Identify the blood parasite species.
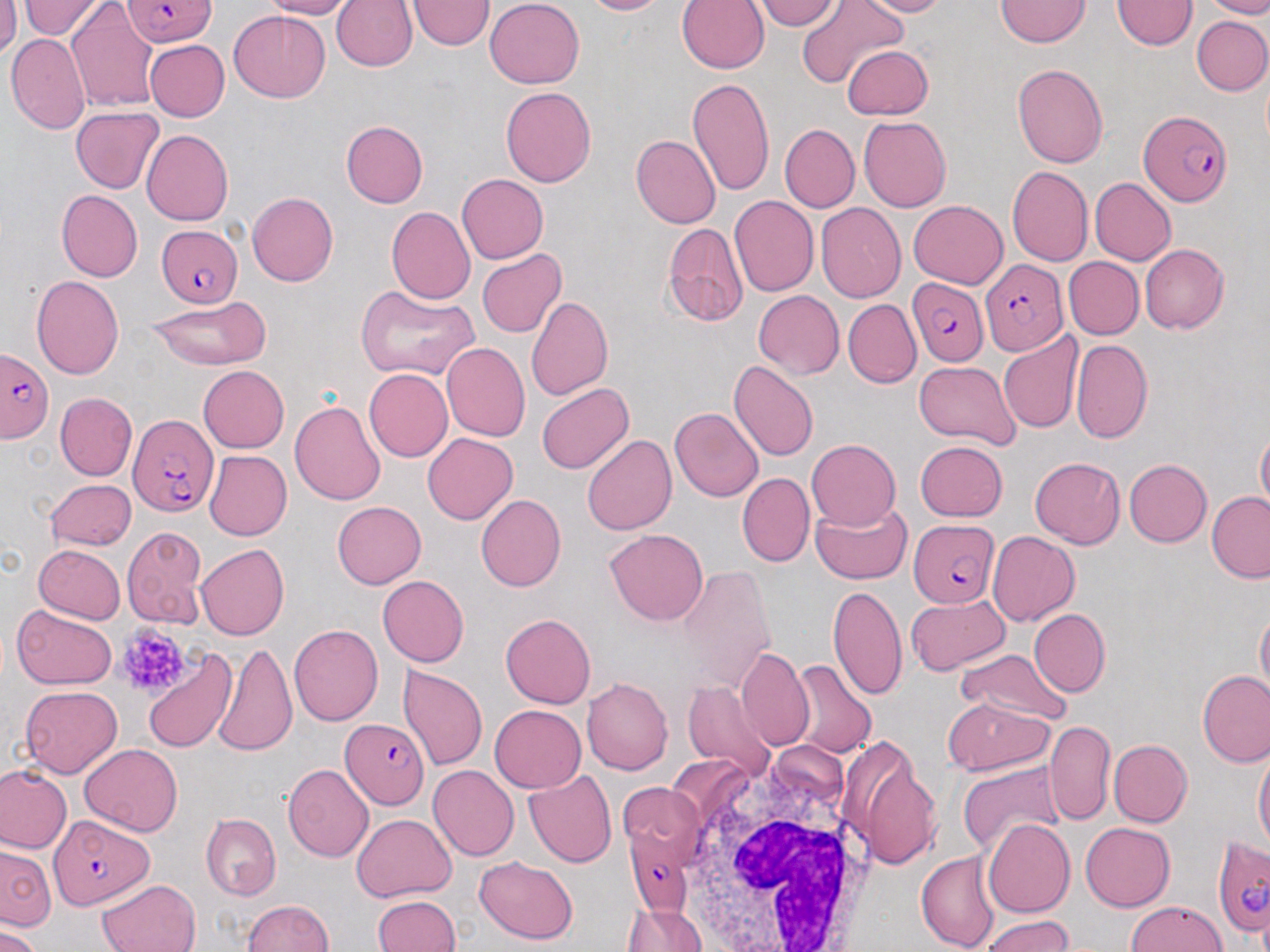
Plasmodium falciparum.

Approximate bounding boxes as (x1, y1, x2, y2) in pixels. Plasmodium falciparum-infected red blood cell locations: (118, 2, 217, 47), (1138, 110, 1234, 207), (154, 223, 243, 308), (981, 259, 1067, 353), (906, 278, 988, 368), (0, 345, 54, 438), (126, 413, 218, 519), (908, 519, 1000, 608), (343, 721, 431, 807), (48, 818, 154, 910), (626, 820, 698, 936), (1213, 837, 1269, 934). Platelet locations: (116, 623, 191, 696). Uninfected red blood cell locations: (17, 0, 106, 42), (261, 0, 355, 18), (330, 0, 417, 73), (410, 0, 490, 50), (581, 0, 673, 18), (676, 0, 769, 74), (754, 0, 844, 30), (858, 0, 956, 16), (996, 0, 1088, 48), (1114, 0, 1195, 52), (1208, 0, 1269, 17), (485, 1, 584, 89), (796, 2, 906, 91), (1, 3, 20, 59), (68, 6, 159, 109), (228, 9, 332, 103), (1191, 15, 1270, 95), (7, 32, 91, 134), (145, 39, 229, 120), (841, 45, 935, 119), (1012, 62, 1107, 168), (687, 78, 774, 196), (500, 85, 596, 189), (73, 106, 164, 192), (860, 114, 953, 213), (342, 122, 428, 207), (778, 123, 860, 215), (141, 130, 234, 224), (630, 136, 719, 229), (1008, 167, 1092, 267), (455, 173, 549, 263), (1089, 178, 1177, 265), (56, 190, 143, 281), (247, 191, 338, 285), (728, 197, 818, 298), (909, 199, 1009, 288), (816, 203, 906, 302), (387, 207, 476, 306), (661, 222, 748, 327), (1140, 244, 1228, 334), (476, 247, 565, 338), (1064, 256, 1144, 337), (31, 272, 125, 380), (354, 284, 481, 384), (753, 291, 845, 379), (146, 296, 273, 368), (525, 298, 616, 401), (842, 299, 921, 390), (998, 331, 1082, 434), (1072, 337, 1153, 443), (441, 342, 530, 442), (914, 360, 1020, 449), (728, 361, 818, 461), (197, 365, 289, 453), (362, 367, 451, 461), (536, 382, 634, 474), (57, 393, 136, 482), (291, 399, 385, 506), (671, 407, 763, 503), (1255, 430, 1269, 514), (423, 433, 517, 524), (581, 433, 677, 537), (806, 438, 900, 531), (915, 440, 1008, 521), (204, 451, 291, 539), (1028, 456, 1125, 549), (1122, 459, 1211, 548), (738, 472, 814, 567), (44, 480, 135, 549), (1207, 491, 1270, 582), (476, 496, 565, 592), (809, 499, 915, 584), (331, 500, 425, 589), (122, 526, 209, 628), (605, 528, 709, 625), (987, 530, 1079, 626), (195, 544, 290, 639), (33, 545, 126, 623), (376, 575, 467, 666), (828, 583, 910, 704), (906, 593, 1013, 675), (11, 606, 119, 688), (1255, 606, 1269, 692), (1029, 609, 1110, 695), (500, 613, 594, 709), (290, 623, 383, 726), (212, 640, 302, 756), (736, 646, 814, 749), (143, 647, 238, 753), (954, 647, 1072, 726), (789, 658, 876, 761), (399, 667, 487, 771), (1198, 672, 1270, 767), (682, 678, 776, 776), (581, 680, 672, 776), (20, 684, 123, 777), (942, 698, 1054, 776), (489, 706, 585, 792), (1045, 719, 1115, 824), (839, 735, 942, 870), (1108, 739, 1192, 828), (80, 744, 181, 836), (1253, 753, 1268, 855), (958, 762, 1068, 857), (0, 763, 69, 854), (283, 764, 373, 863), (427, 765, 518, 859), (526, 771, 619, 867), (617, 783, 705, 856), (199, 813, 281, 900), (351, 813, 457, 902), (981, 817, 1075, 920), (1078, 822, 1174, 912), (1, 845, 56, 934), (916, 850, 1000, 952), (475, 856, 576, 943), (96, 878, 199, 952), (372, 895, 463, 952), (241, 898, 338, 952), (1123, 898, 1229, 952), (626, 902, 708, 952), (978, 912, 1078, 952), (0, 928, 44, 952). White blood cell locations: (660, 738, 871, 952). 1000x magnification. Optical microscopy. Image is 1270×952 pixels. May-Grünwald-Giemsa stain. Thin blood smear. Single field of view.